Assess the morphology of the erythrocytes.
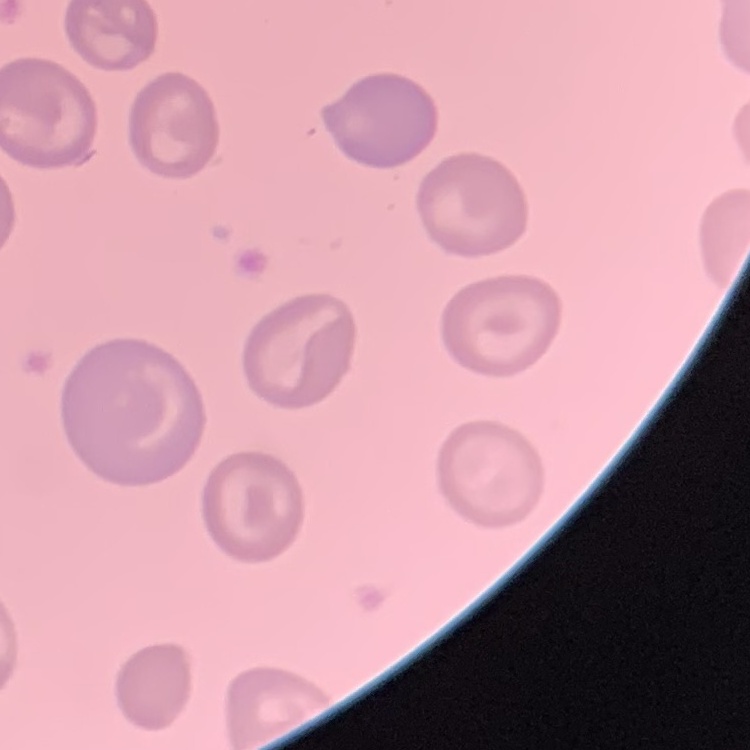
No rouleaux formation.

image type = one tile cut from a larger photomicrograph
stain = Field's or Giemsa
preparation = thin blood film